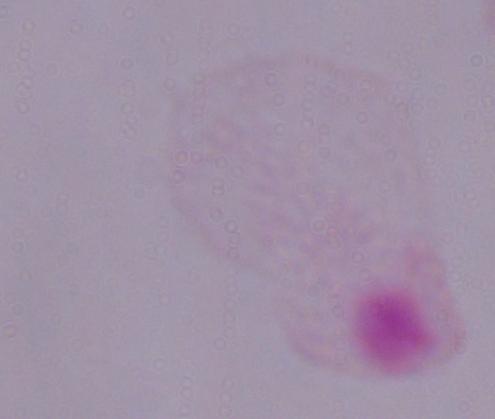
{
  "identification": "trichomonad",
  "modality": "photomicrograph",
  "magnification": "1000x"
}